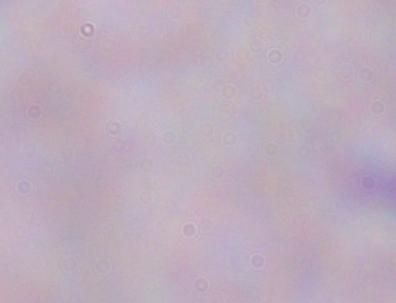 A trypanosome is seen. Photomicrograph. Captured at 1000x magnification.